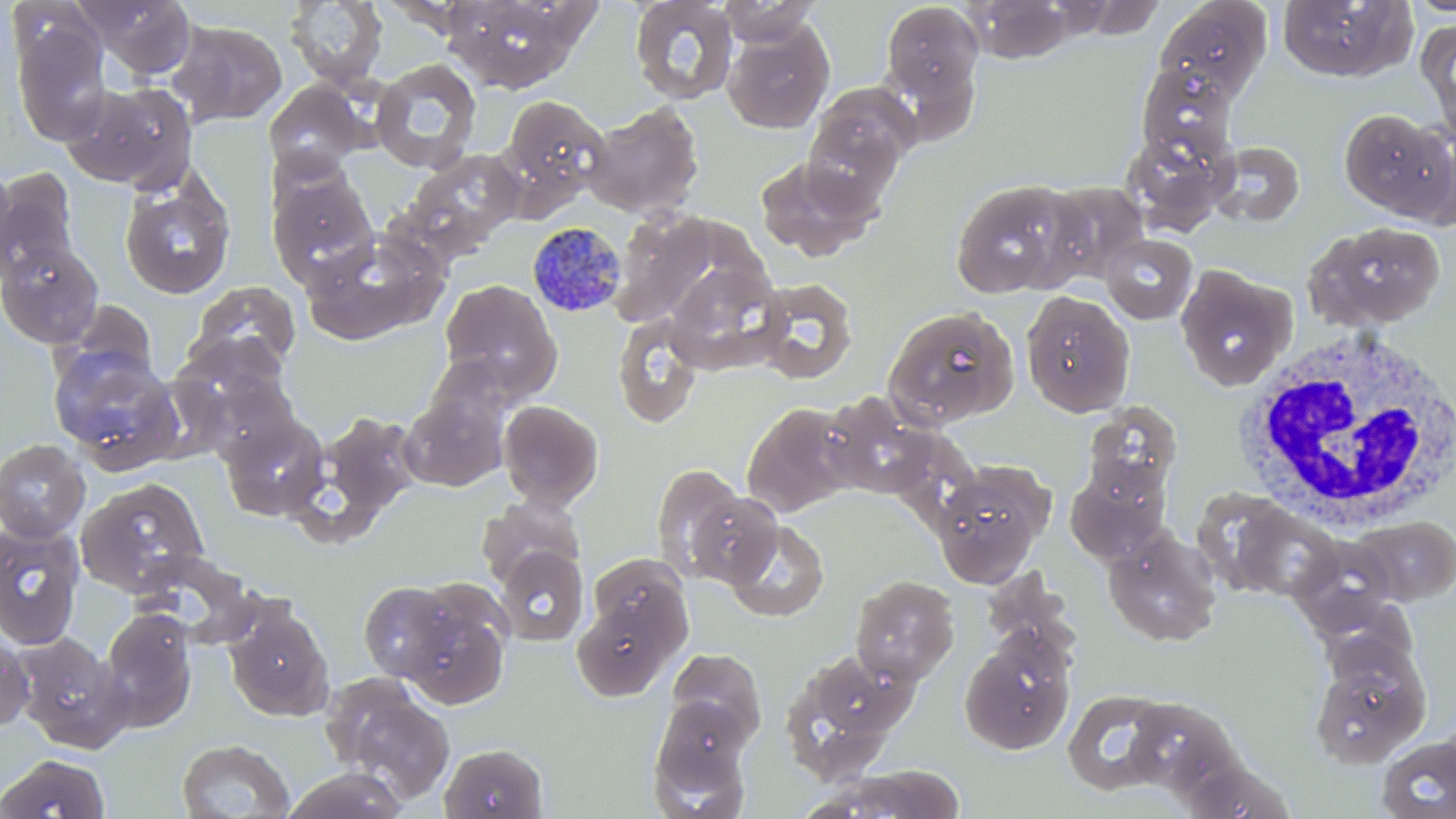

Approximate bounding boxes as (x1, y1, x2, y2) in pixels. White blood cell locations: (1233, 326, 1456, 527). Plasmodium malariae-infected red blood cell locations: (527, 221, 629, 318). Uninfected red blood cell locations: (73, 0, 199, 80), (447, 0, 578, 92), (629, 0, 738, 105), (717, 0, 823, 46), (880, 0, 985, 111), (966, 0, 1072, 63), (1153, 0, 1273, 101), (1276, 0, 1415, 81), (1406, 0, 1456, 19), (286, 1, 387, 89), (11, 16, 112, 146), (1417, 17, 1456, 132), (172, 20, 287, 126), (722, 23, 833, 134), (369, 56, 482, 173), (1136, 63, 1236, 159), (264, 81, 368, 177), (60, 83, 194, 192), (802, 84, 919, 203), (497, 94, 613, 216), (583, 101, 705, 219), (1339, 108, 1453, 222), (1122, 132, 1230, 234), (1210, 140, 1305, 228), (402, 149, 525, 255), (753, 156, 876, 260), (0, 165, 18, 275), (1, 167, 79, 280), (267, 169, 379, 284), (119, 172, 236, 300), (948, 180, 1082, 297), (1039, 182, 1148, 285), (1304, 221, 1447, 330), (300, 231, 444, 344), (1101, 234, 1198, 323), (0, 242, 103, 348), (664, 264, 784, 370), (1175, 264, 1296, 392), (753, 278, 859, 383), (439, 279, 562, 399), (189, 281, 301, 374), (1020, 291, 1135, 417), (883, 306, 1021, 431), (612, 315, 704, 428), (174, 332, 290, 425), (48, 345, 182, 473), (191, 370, 302, 465), (400, 392, 508, 491), (818, 393, 944, 499), (497, 399, 604, 509), (741, 402, 857, 518), (1081, 403, 1182, 502), (317, 411, 423, 521), (221, 414, 330, 523), (0, 439, 91, 542), (932, 460, 1054, 586), (651, 463, 748, 578), (1066, 464, 1170, 563), (76, 477, 210, 596), (682, 491, 783, 588), (477, 494, 585, 588), (1232, 504, 1344, 601), (1351, 516, 1456, 605), (724, 519, 830, 622), (0, 521, 84, 649), (1103, 529, 1222, 647), (1284, 534, 1404, 635), (494, 547, 590, 645), (134, 551, 259, 645), (589, 554, 689, 642), (850, 575, 959, 685), (358, 581, 460, 682), (396, 583, 513, 709), (221, 596, 335, 723), (1317, 597, 1434, 687), (571, 599, 677, 701), (100, 608, 198, 731), (961, 629, 1077, 755), (0, 631, 34, 735), (11, 631, 131, 753), (666, 648, 768, 746), (1308, 648, 1432, 769), (779, 650, 913, 776), (320, 674, 456, 806), (1063, 689, 1176, 795), (1132, 699, 1245, 799), (648, 700, 752, 813), (1376, 735, 1456, 819), (177, 738, 295, 818), (440, 742, 548, 819), (2, 752, 111, 818), (284, 766, 409, 819), (804, 767, 966, 819). Slide-level diagnosis: Plasmodium malariae. Single field of view. Captured at 1000x magnification. Thin blood smear. Optical microscopy. May-Grünwald-Giemsa-stained preparation. Image is 1456×819 pixels.